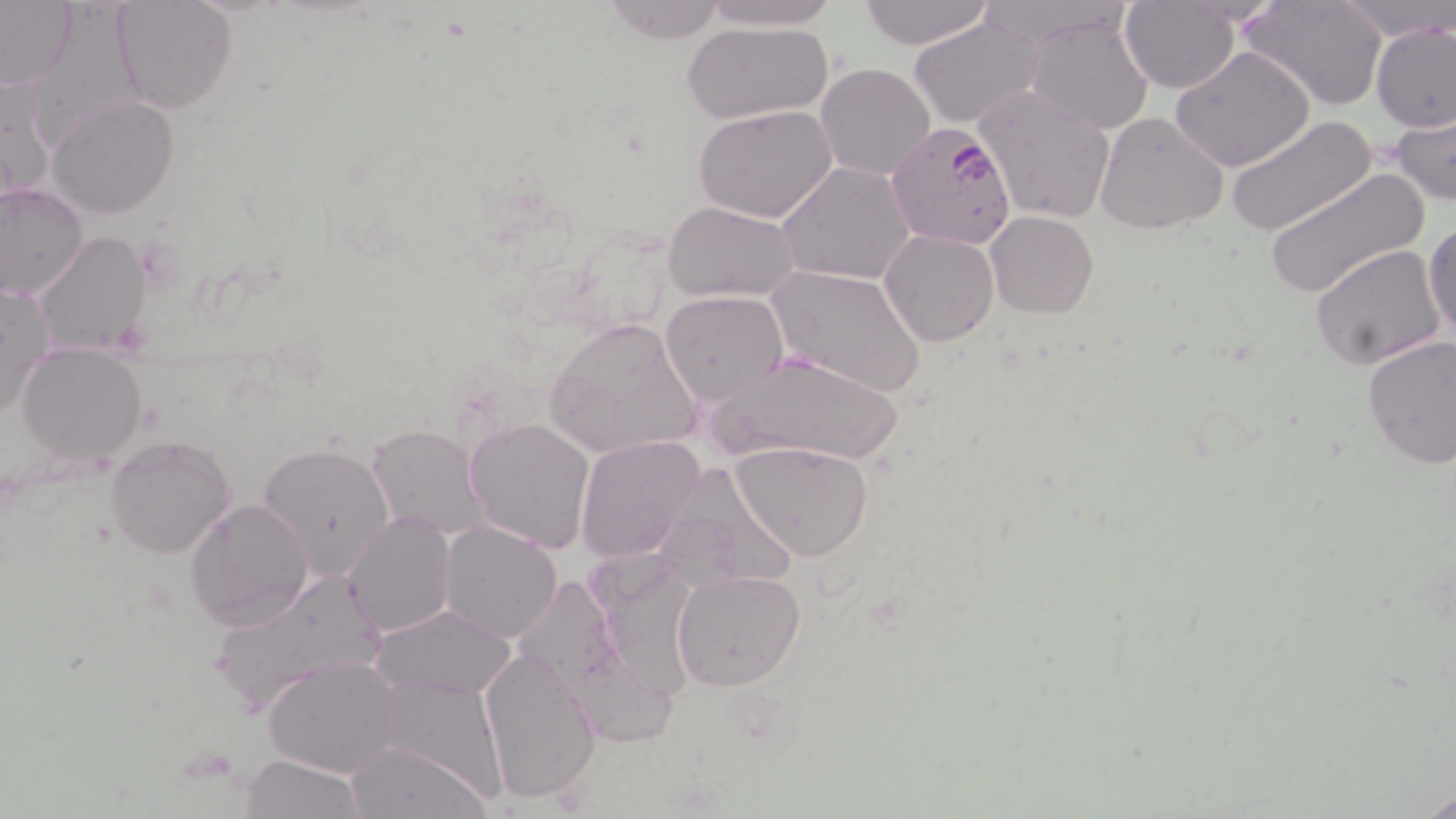
Summary:
  - Coordinate format: approximate bounding boxes as (x1,y1)-(x2,y2) corner pairs in pixels
  - Uninfected red blood cell locations: (111,0)-(236,114), (694,0)-(845,31), (856,0)-(996,50), (1241,0)-(1388,111), (1333,0)-(1453,41), (0,1)-(79,91), (600,1)-(731,44), (1120,1)-(1241,93), (1026,10)-(1153,136), (908,16)-(1048,129), (682,21)-(832,126), (1370,22)-(1454,131), (1173,45)-(1317,173), (816,63)-(936,181), (1,71)-(59,203), (971,83)-(1118,226), (46,95)-(181,220), (694,104)-(840,223), (1391,107)-(1455,206), (1095,112)-(1229,235), (1228,115)-(1378,239), (776,162)-(917,286), (1263,169)-(1429,298), (0,182)-(88,301), (663,201)-(801,302), (986,210)-(1098,320), (1424,217)-(1456,350), (880,229)-(999,347), (35,232)-(152,356), (1310,244)-(1448,372), (768,263)-(926,398), (1,282)-(53,420), (660,290)-(787,408), (545,315)-(704,459), (1360,333)-(1456,469), (16,342)-(147,465), (709,348)-(908,466), (464,418)-(595,553), (366,424)-(489,543), (105,433)-(235,558), (574,437)-(705,564), (731,441)-(874,561), (258,442)-(399,580), (651,462)-(802,593), (184,497)-(314,632), (342,509)-(456,638), (438,520)-(563,643), (206,567)-(389,716), (671,569)-(805,692), (372,604)-(517,700), (478,646)-(602,806), (263,655)-(404,777), (346,740)-(493,819), (241,755)-(365,818), (1419,786)-(1456,819)
  - Plasmodium falciparum-infected red blood cell locations: (885,120)-(1018,250)
  - Slide-level diagnosis: Plasmodium falciparum
  - Image size: 1456×819 pixels
  - Magnification: 1000x
  - Field of view: one of a larger specimen
  - Modality: light microscopy
  - Stain: May-Grünwald-Giemsa
  - Preparation: thin blood film